Comment on the morphology of the erythrocytes.
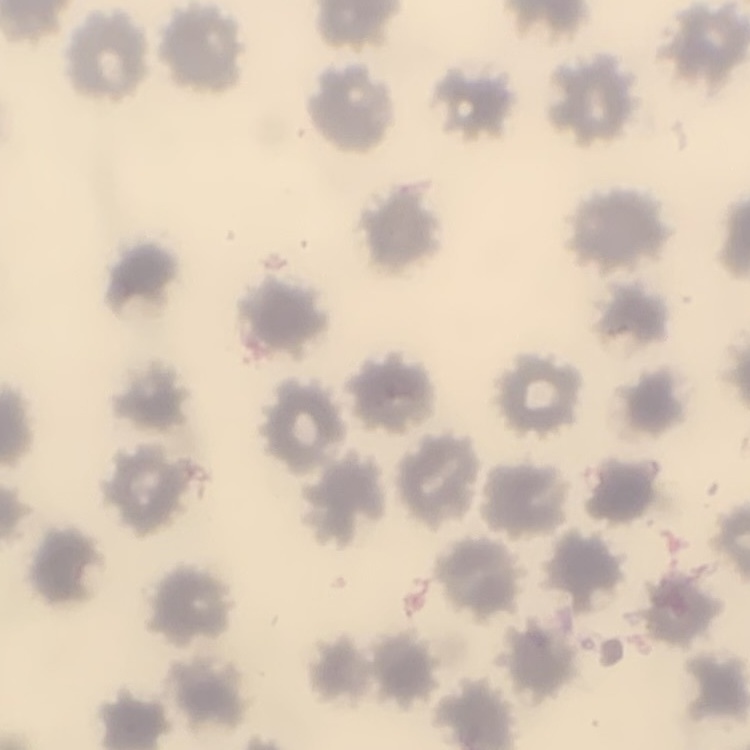

They show no rouleaux formation.

Summary:
  - Preparation: thin blood film
  - Stain: Field's or Giemsa
  - Image type: square crop of a larger photomicrograph